Locate and identify every blood parasite.
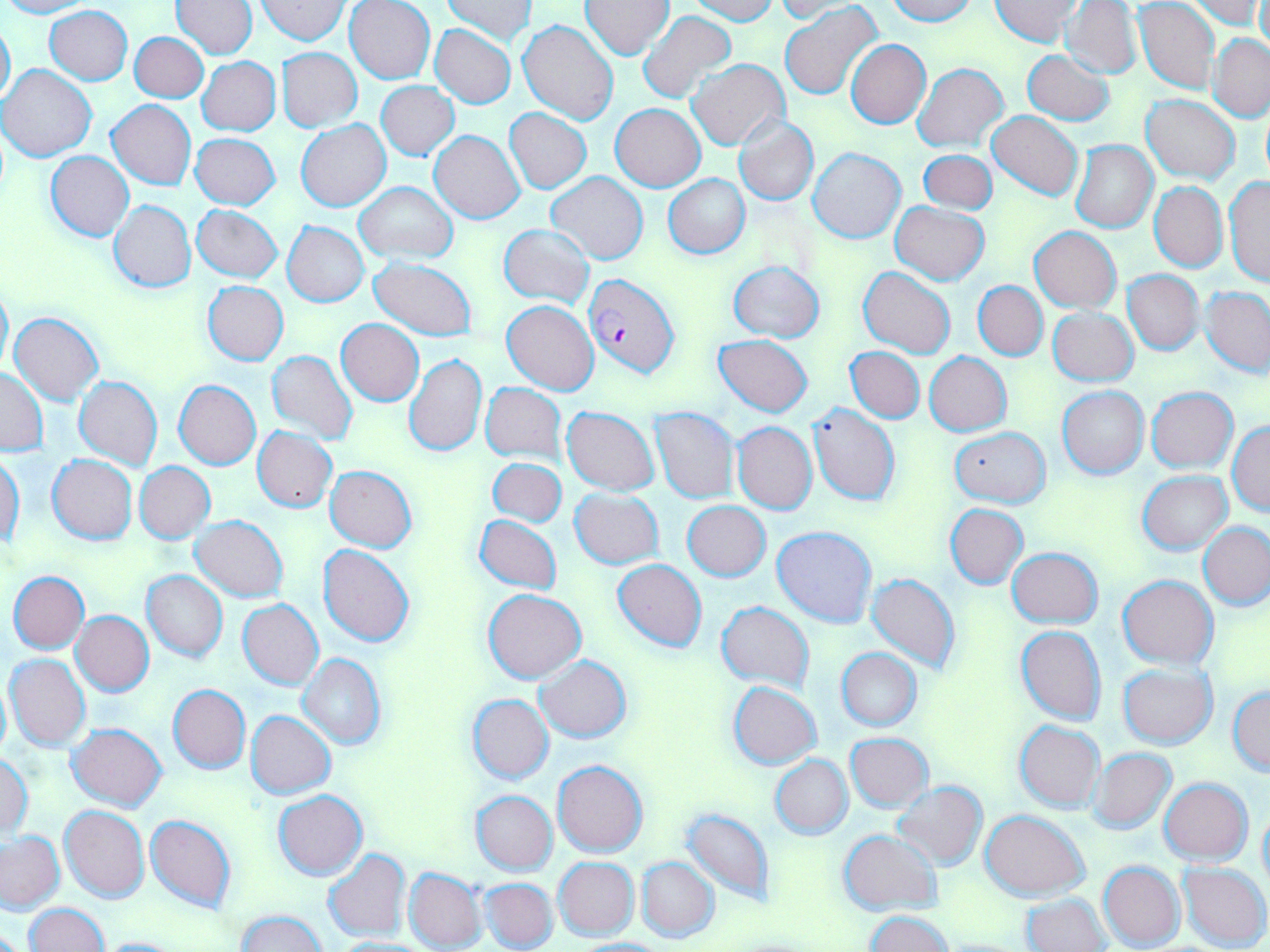
Approximate bounding boxes as [x1, y1, x2, y2] in pixels.
Plasmodium falciparum-infected red blood cells: [583, 273, 678, 378].
No Plasmodium ovale, Plasmodium malariae, Plasmodium vivax, Babesia divergens, or Trypanosoma brucei observed.

Uninfected red blood cell locations: [0, 0, 92, 18], [345, 0, 434, 85], [443, 0, 537, 45], [688, 0, 776, 24], [884, 0, 976, 25], [989, 0, 1084, 47], [1183, 0, 1263, 29], [1257, 0, 1270, 58], [172, 1, 258, 57], [255, 1, 350, 44], [582, 1, 673, 59], [1063, 1, 1142, 79], [774, 2, 857, 22], [781, 2, 885, 100], [1134, 2, 1220, 94], [44, 6, 133, 85], [639, 10, 737, 103], [0, 16, 15, 109], [517, 20, 618, 125], [430, 25, 516, 108], [130, 32, 209, 102], [1209, 34, 1270, 121], [846, 39, 931, 128], [276, 48, 363, 132], [1021, 49, 1115, 125], [197, 56, 280, 135], [687, 59, 790, 151], [912, 63, 1010, 151], [0, 64, 96, 162], [376, 81, 459, 159], [1141, 94, 1240, 184], [107, 99, 196, 190], [611, 104, 705, 192], [505, 109, 591, 193], [987, 112, 1083, 201], [734, 117, 819, 205], [296, 119, 391, 211], [429, 130, 525, 223], [190, 133, 280, 210], [1070, 140, 1159, 233], [808, 146, 905, 242], [919, 150, 997, 213], [46, 151, 134, 240], [546, 172, 649, 264], [663, 174, 749, 259], [1224, 177, 1270, 289], [1149, 181, 1227, 273], [355, 182, 457, 262], [108, 200, 196, 293], [890, 202, 990, 285], [192, 205, 283, 282], [282, 221, 368, 307], [499, 224, 594, 307], [1030, 226, 1121, 313], [369, 257, 477, 339], [729, 260, 825, 342], [858, 267, 956, 359], [1122, 270, 1204, 355], [0, 280, 11, 379], [202, 281, 289, 365], [973, 281, 1048, 360], [1202, 286, 1270, 376], [501, 300, 599, 394], [1048, 307, 1138, 385], [10, 311, 104, 405], [336, 319, 423, 405], [715, 335, 812, 417], [845, 347, 924, 423], [267, 350, 359, 446], [925, 351, 1012, 436], [403, 355, 487, 456], [0, 367, 47, 456], [74, 375, 162, 470], [174, 380, 261, 469], [481, 382, 566, 462], [1057, 386, 1150, 479], [1147, 387, 1238, 472], [807, 403, 901, 505], [562, 406, 659, 495], [650, 407, 741, 504], [1228, 421, 1269, 515], [732, 422, 816, 514], [950, 426, 1050, 507], [253, 427, 338, 512], [1, 451, 24, 551], [46, 455, 137, 545], [488, 457, 567, 527], [135, 462, 215, 545], [325, 465, 417, 552], [1138, 472, 1231, 554], [570, 488, 664, 569], [683, 502, 770, 582], [946, 504, 1029, 589], [474, 514, 561, 594], [190, 516, 289, 601], [1199, 521, 1269, 610], [771, 526, 878, 627], [318, 544, 416, 647], [1007, 547, 1102, 627], [613, 560, 708, 653], [142, 570, 228, 663], [9, 571, 89, 654], [867, 573, 961, 674], [1119, 576, 1219, 668], [483, 588, 587, 684], [238, 599, 324, 689], [717, 601, 814, 690], [72, 611, 154, 696], [1015, 625, 1107, 726], [835, 648, 922, 730], [5, 654, 91, 752], [297, 654, 385, 751], [534, 656, 631, 742], [1117, 662, 1217, 749], [0, 674, 11, 762], [728, 682, 821, 768], [168, 684, 250, 774], [1227, 688, 1270, 776], [467, 694, 553, 785], [246, 710, 335, 800], [1015, 720, 1104, 812], [67, 723, 167, 811], [845, 733, 935, 812], [1089, 748, 1177, 834], [0, 755, 34, 840], [771, 755, 853, 839], [553, 760, 647, 857], [1160, 778, 1253, 864], [892, 782, 987, 869], [471, 790, 557, 875], [273, 791, 367, 880], [60, 805, 149, 902], [1258, 807, 1270, 891], [681, 808, 774, 903], [980, 810, 1090, 902], [145, 813, 237, 913], [838, 829, 942, 915], [0, 831, 65, 913], [323, 849, 411, 942], [636, 856, 719, 943], [553, 857, 639, 940], [1098, 861, 1185, 950], [1178, 861, 1270, 950], [405, 867, 488, 950], [479, 878, 558, 951], [1023, 894, 1109, 952], [26, 902, 107, 951], [237, 910, 327, 951], [865, 911, 955, 952], [91, 936, 187, 952], [332, 938, 436, 951], [572, 939, 672, 952]. Slide-level diagnosis: Plasmodium falciparum. Single field of view. Thin blood smear. May-Grünwald-Giemsa-stained preparation. Captured at 1000x magnification. Image is 1270×952 pixels. Light microscopy.